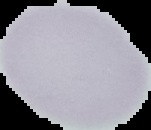

Summary:
  - Preparation: thin blood smear
  - Image size: 151×130 pixels
  - Image type: segmented cell region with the area outside set to black
  - Result: no malaria parasites detected